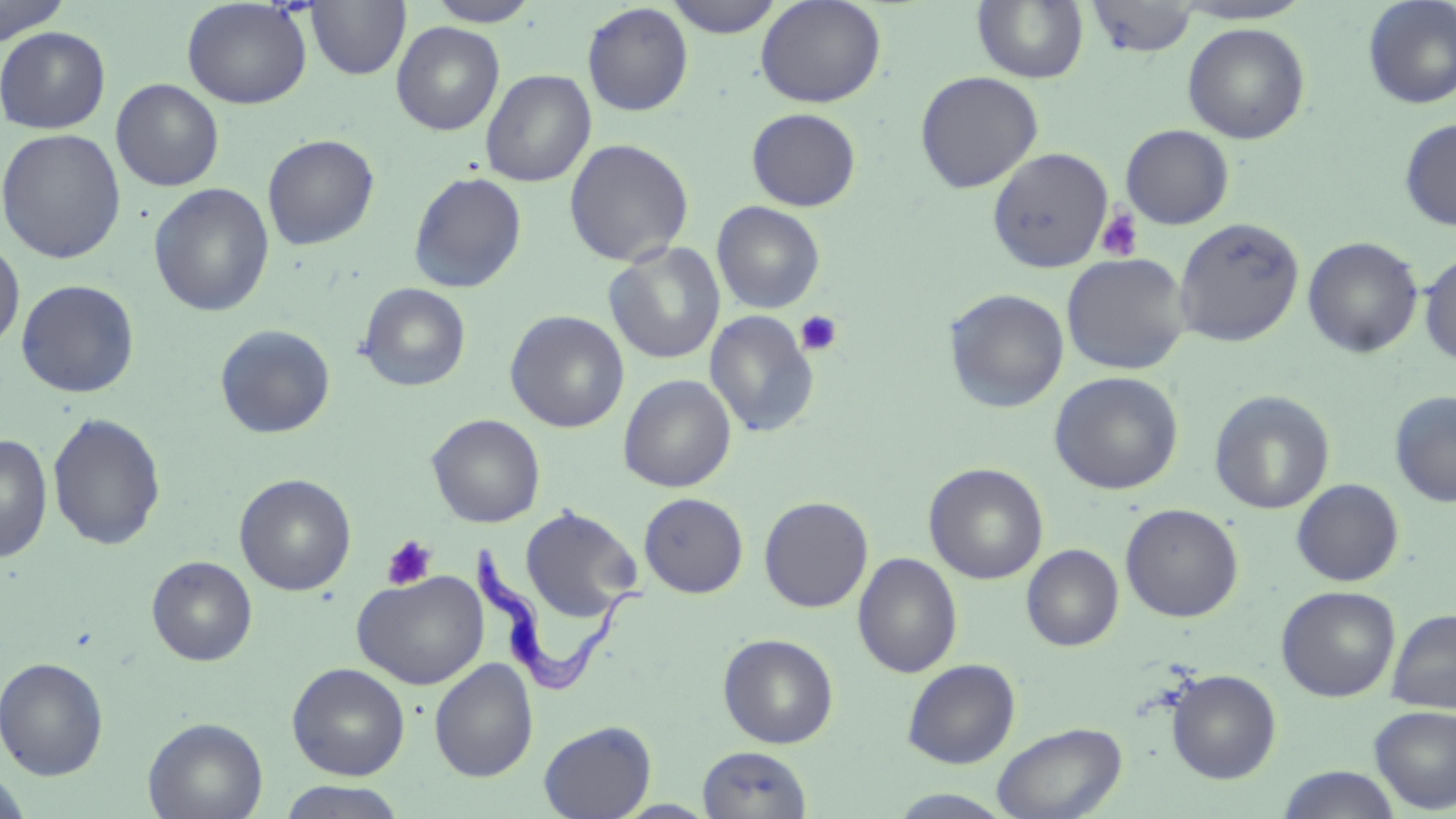
Approximate bounding boxes as (x1, y1, x2, y2) in pixels. Platelet locations: (1095, 208, 1143, 261), (794, 310, 843, 357), (381, 534, 438, 591). Trypanosoma brucei locations: (468, 542, 649, 695). Uninfected red blood cell locations: (0, 0, 71, 44), (182, 0, 312, 109), (306, 0, 410, 80), (664, 0, 785, 39), (755, 0, 886, 108), (973, 0, 1089, 84), (1085, 0, 1199, 58), (1361, 0, 1456, 109), (425, 1, 540, 26), (582, 3, 693, 116), (391, 22, 505, 136), (1182, 22, 1310, 144), (0, 26, 110, 134), (481, 69, 596, 187), (914, 71, 1043, 193), (111, 79, 224, 191), (746, 108, 861, 211), (1399, 117, 1456, 231), (1120, 124, 1234, 230), (1, 128, 126, 264), (262, 134, 380, 250), (564, 138, 694, 267), (987, 147, 1114, 274), (409, 171, 527, 294), (149, 183, 275, 317), (712, 201, 825, 314), (1174, 216, 1304, 347), (1303, 236, 1424, 358), (0, 237, 25, 354), (604, 242, 725, 364), (1418, 251, 1456, 365), (1061, 253, 1191, 375), (16, 279, 140, 398), (357, 283, 471, 392), (944, 288, 1069, 414), (505, 310, 629, 433), (704, 310, 819, 438), (214, 323, 336, 439), (1049, 371, 1184, 495), (618, 374, 737, 492), (1209, 389, 1335, 514), (1389, 391, 1456, 507), (47, 412, 166, 552), (427, 414, 545, 527), (0, 433, 53, 563), (923, 463, 1049, 584), (234, 474, 356, 596), (1291, 479, 1404, 587), (639, 492, 748, 598), (759, 496, 873, 613), (1120, 503, 1243, 622), (520, 506, 642, 622), (1022, 544, 1123, 651), (852, 553, 963, 678), (147, 555, 257, 666), (351, 570, 488, 690), (1276, 586, 1400, 702), (1387, 608, 1456, 713), (718, 633, 839, 748), (0, 657, 109, 780), (902, 658, 1020, 768), (429, 659, 539, 781), (287, 662, 410, 780), (1166, 669, 1281, 784), (1370, 705, 1456, 814), (143, 717, 268, 819), (538, 720, 656, 819), (992, 721, 1127, 819), (698, 745, 812, 818), (1276, 766, 1403, 819), (0, 771, 33, 819), (276, 781, 410, 819), (886, 789, 1018, 818). Slide-level diagnosis: Trypanosoma brucei. Image is 1456×819 pixels. Thin blood smear. One field of a larger specimen. Optical microscopy. May-Grünwald-Giemsa stain. 1000x magnification.